Identify the parasite.
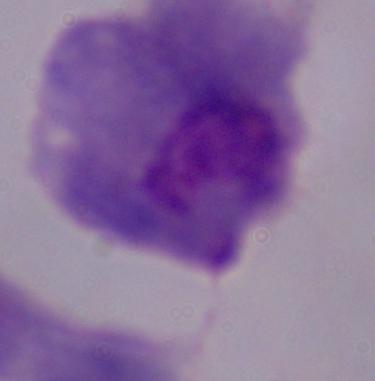

A trichomonad.

Captured at 1000x magnification. Photomicrograph.